Classify this cell by malaria status.
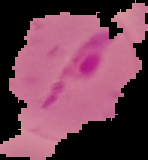

Parasitized.

The area outside the segmented cell region is set to black. From a thin blood smear. Image is 148×160 pixels.